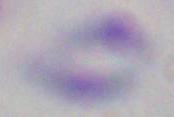
modality = photomicrograph
magnification = 1000x
identification = Toxoplasma gondii